Identify the parasite.
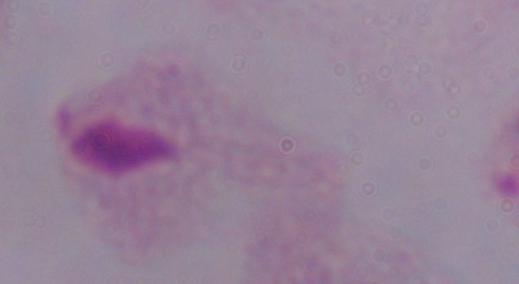
A trichomonad.

Photomicrograph. 1000x magnification.